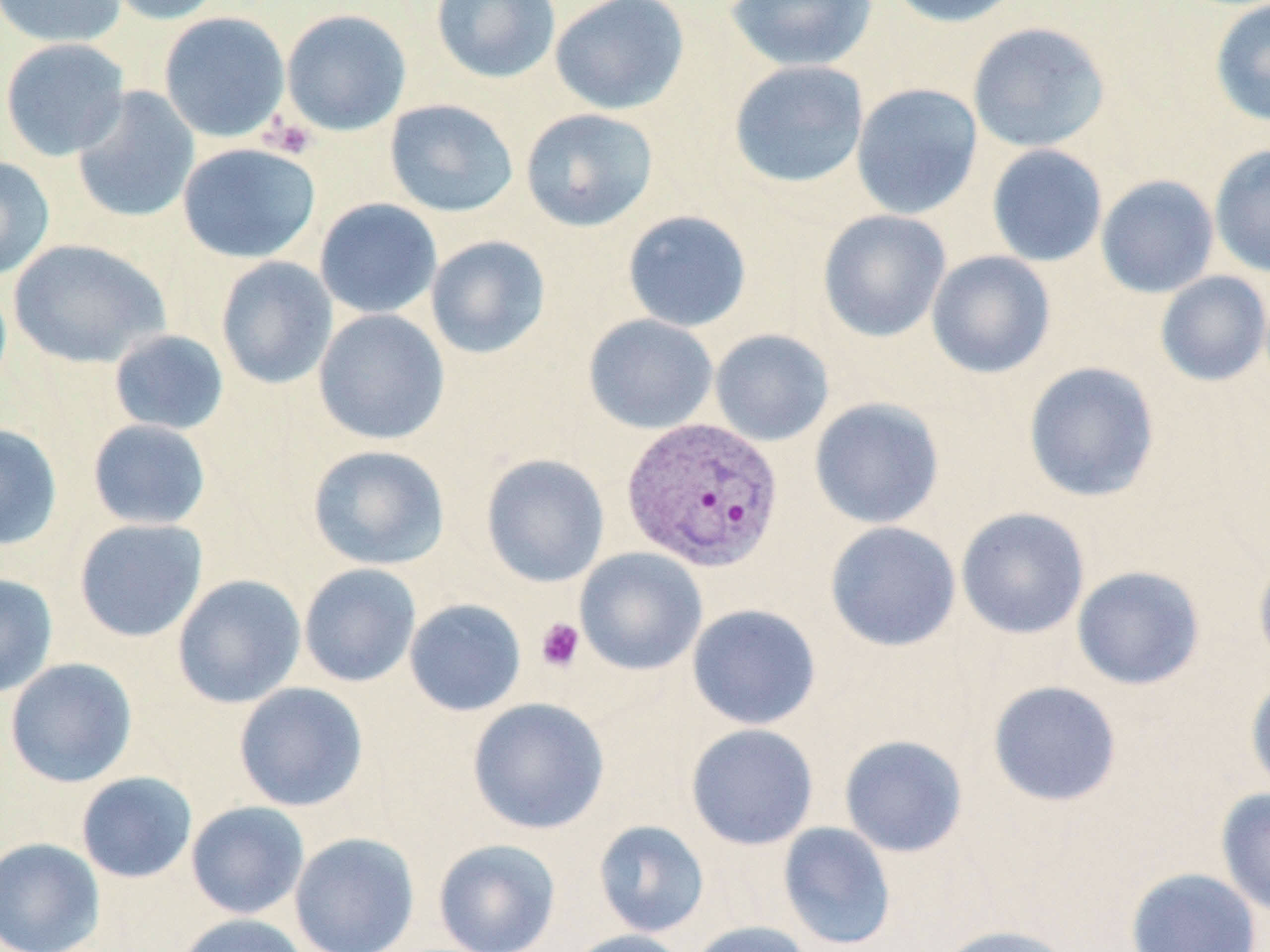
Summary:
  - Coordinate format: approximate bounding boxes as [x1, y1, x2, y2] in pixels
  - Uninfected red blood cell locations: [0, 0, 127, 48], [103, 0, 226, 25], [430, 0, 561, 84], [549, 0, 690, 116], [725, 0, 878, 72], [884, 0, 1024, 27], [1209, 1, 1270, 126], [281, 9, 411, 136], [158, 12, 290, 143], [967, 21, 1111, 153], [1, 37, 131, 161], [728, 60, 869, 190], [851, 83, 983, 219], [72, 87, 200, 224], [384, 99, 519, 218], [520, 108, 659, 232], [177, 142, 321, 264], [1209, 143, 1270, 278], [986, 144, 1108, 267], [0, 156, 55, 281], [1095, 174, 1219, 298], [314, 198, 442, 319], [622, 210, 752, 332], [817, 210, 952, 342], [425, 235, 551, 359], [8, 238, 170, 368], [926, 250, 1056, 379], [215, 257, 338, 389], [1154, 271, 1270, 386], [313, 309, 450, 445], [583, 314, 718, 434], [108, 329, 229, 435], [709, 329, 834, 446], [1023, 361, 1160, 503], [809, 397, 945, 528], [87, 419, 212, 530], [0, 422, 63, 551], [307, 445, 450, 570], [480, 454, 610, 587], [955, 507, 1090, 639], [74, 518, 208, 642], [824, 521, 961, 652], [574, 547, 708, 676], [1253, 549, 1270, 674], [299, 563, 422, 688], [1071, 565, 1206, 690], [0, 573, 59, 699], [171, 574, 306, 709], [404, 599, 527, 716], [687, 603, 821, 730], [4, 657, 137, 788], [1245, 674, 1270, 797], [987, 680, 1122, 808], [233, 682, 369, 812], [467, 697, 610, 834], [685, 723, 819, 850], [839, 734, 969, 858], [76, 771, 197, 884], [1216, 787, 1270, 919], [185, 801, 309, 920], [592, 820, 710, 937], [778, 822, 897, 950], [289, 832, 420, 952], [0, 837, 106, 952], [432, 838, 562, 952], [1125, 867, 1262, 952], [175, 913, 311, 952], [687, 920, 814, 952], [933, 924, 1075, 952], [561, 929, 694, 952]
  - Plasmodium vivax-infected red blood cell locations: [621, 417, 784, 573]
  - Platelet locations: [263, 117, 317, 159], [535, 617, 585, 672]
  - Slide-level diagnosis: Plasmodium vivax
  - Field of view: single
  - Modality: light microscopy
  - Preparation: thin blood smear
  - Stain: May-Grünwald-Giemsa
  - Image size: 1270×952 pixels
  - Magnification: 1000x